Assess this cell for malaria.
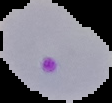
Parasitized.

Summary:
  - Preparation: thin blood smear
  - Image size: 112×103 pixels
  - Image type: segmented cell region with the area outside set to black